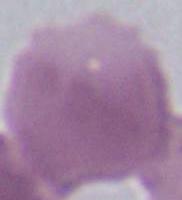
{
  "magnification": "1000x",
  "identification": "erythrocyte",
  "modality": "micrograph"
}